Locate and identify every blood parasite.
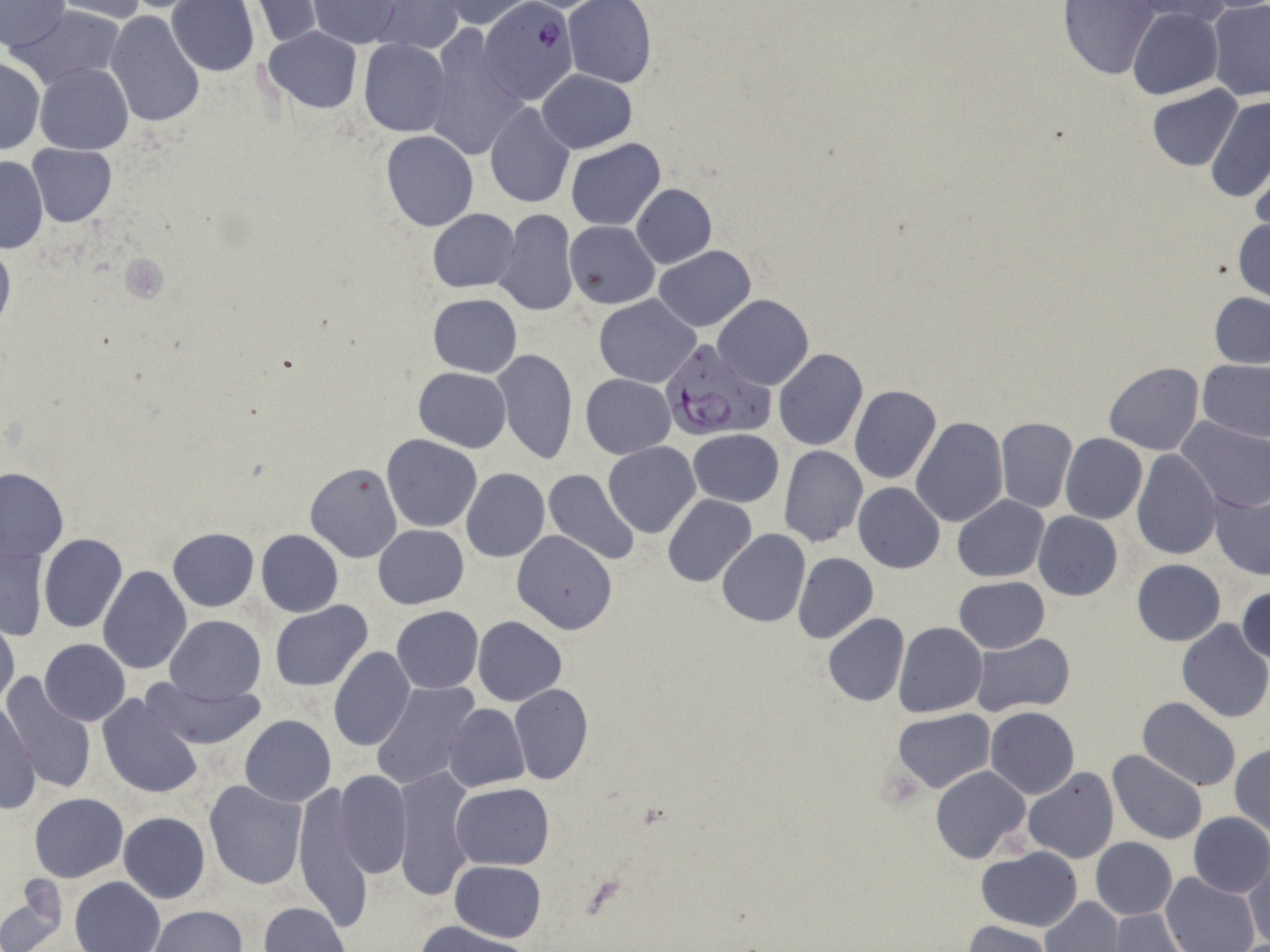
Approximate bounding boxes as (x1, y1, x2, y2) in pixels.
Plasmodium falciparum-infected red blood cells: (482, 1, 578, 104), (660, 340, 771, 444).
No Plasmodium ovale, Plasmodium malariae, Plasmodium vivax, Babesia divergens, or Trypanosoma brucei observed.

Summary:
  - Platelet locations: (121, 253, 169, 304)
  - Uninfected red blood cell locations: (51, 0, 151, 22), (0, 1, 70, 50), (168, 1, 260, 75), (250, 1, 326, 47), (309, 1, 404, 48), (373, 1, 464, 54), (438, 1, 535, 27), (565, 1, 656, 87), (1125, 1, 1239, 25), (1054, 2, 1161, 80), (12, 4, 128, 89), (1208, 4, 1270, 101), (1128, 8, 1223, 99), (105, 10, 204, 127), (263, 26, 362, 113), (422, 29, 527, 159), (357, 38, 451, 137), (0, 57, 44, 154), (35, 63, 133, 154), (538, 69, 637, 153), (1148, 85, 1242, 170), (1206, 96, 1270, 203), (484, 102, 575, 208), (381, 131, 479, 231), (565, 138, 665, 231), (27, 144, 116, 226), (0, 157, 48, 251), (1248, 157, 1269, 244), (631, 183, 716, 269), (427, 209, 518, 292), (493, 210, 580, 317), (1233, 217, 1269, 302), (567, 220, 660, 309), (0, 239, 14, 333), (654, 246, 756, 331), (1209, 292, 1270, 369), (428, 293, 521, 377), (594, 295, 699, 388), (713, 295, 814, 390), (490, 348, 578, 463), (774, 350, 868, 452), (1197, 358, 1270, 443), (1103, 363, 1204, 455), (414, 367, 512, 451), (581, 374, 676, 458), (848, 384, 941, 485), (911, 416, 1008, 526), (995, 416, 1076, 513), (1175, 416, 1270, 513), (687, 430, 784, 507), (1060, 434, 1147, 524), (382, 435, 483, 532), (603, 441, 700, 538), (778, 446, 867, 546), (1131, 450, 1221, 561), (305, 462, 403, 562), (0, 467, 69, 562), (461, 468, 549, 561), (544, 469, 641, 566), (854, 482, 945, 573), (1211, 491, 1270, 579), (662, 494, 755, 587), (953, 495, 1048, 582), (537, 499, 636, 608), (1033, 512, 1122, 600), (382, 524, 473, 695), (374, 525, 468, 608), (167, 527, 258, 611), (256, 529, 344, 616), (718, 529, 810, 627), (512, 531, 616, 634), (39, 533, 127, 634), (1, 543, 49, 642), (793, 552, 878, 643), (1132, 559, 1225, 645), (98, 566, 192, 675), (954, 577, 1049, 653), (943, 580, 1058, 715), (1237, 584, 1270, 665), (270, 600, 373, 691), (391, 605, 484, 692), (823, 614, 909, 706), (166, 615, 266, 703), (0, 616, 19, 715), (473, 617, 566, 706), (1176, 620, 1270, 721), (894, 622, 987, 717), (970, 633, 1077, 717), (40, 638, 130, 725), (328, 648, 414, 753), (3, 673, 95, 796), (141, 676, 265, 751), (371, 679, 480, 789), (509, 683, 593, 784), (98, 694, 203, 797), (1139, 697, 1242, 792), (1, 701, 39, 813), (444, 703, 529, 792), (985, 707, 1079, 798), (894, 708, 993, 793), (240, 714, 336, 805), (1231, 743, 1270, 837), (1107, 749, 1208, 844), (930, 765, 1031, 864), (392, 767, 475, 901), (1022, 768, 1119, 863), (333, 770, 413, 879), (204, 779, 306, 888), (292, 781, 372, 933), (452, 783, 553, 869), (29, 793, 129, 881), (118, 811, 210, 903), (1187, 812, 1270, 897), (1090, 836, 1177, 919), (978, 846, 1082, 931), (1244, 855, 1269, 948), (450, 860, 545, 942), (1162, 872, 1261, 952), (70, 876, 165, 952), (0, 890, 66, 950), (1044, 896, 1122, 951), (257, 902, 350, 952), (147, 905, 246, 952), (1109, 909, 1187, 952), (414, 921, 530, 952), (963, 921, 1052, 952)
  - Slide-level diagnosis: Plasmodium falciparum
  - Preparation: thin blood smear
  - Field of view: single
  - Image size: 1270×952 pixels
  - Stain: May-Grünwald-Giemsa
  - Modality: optical microscopy
  - Magnification: 1000x